Classify this cell by malaria status.
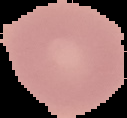

Uninfected.

Summary:
  - Image type: segmented cell region with the area outside set to black
  - Preparation: thin blood film
  - Image size: 127×118 pixels